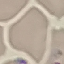

result: negative for malaria parasites
stain: Giemsa
preparation: thin smear
image_type: automatically extracted cell patch, resized to 64 × 64 pixels
capture: smartphone camera at the microscope eyepiece